Assess this cell for malaria.
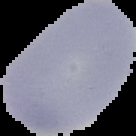

Uninfected.

preparation: thin blood smear
image_size: 136×136 pixels
image_type: segmented cell region with the area outside set to black